Assess this cell for malaria.
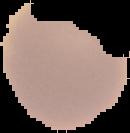
Uninfected.

image size = 130×133 pixels
image type = cell region segmented out of the field of view; surrounding area masked to black
preparation = thin blood film